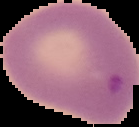
preparation = thin blood smear
image size = 139×127 pixels
malaria status = parasitized
image type = segmented cell region on a black background